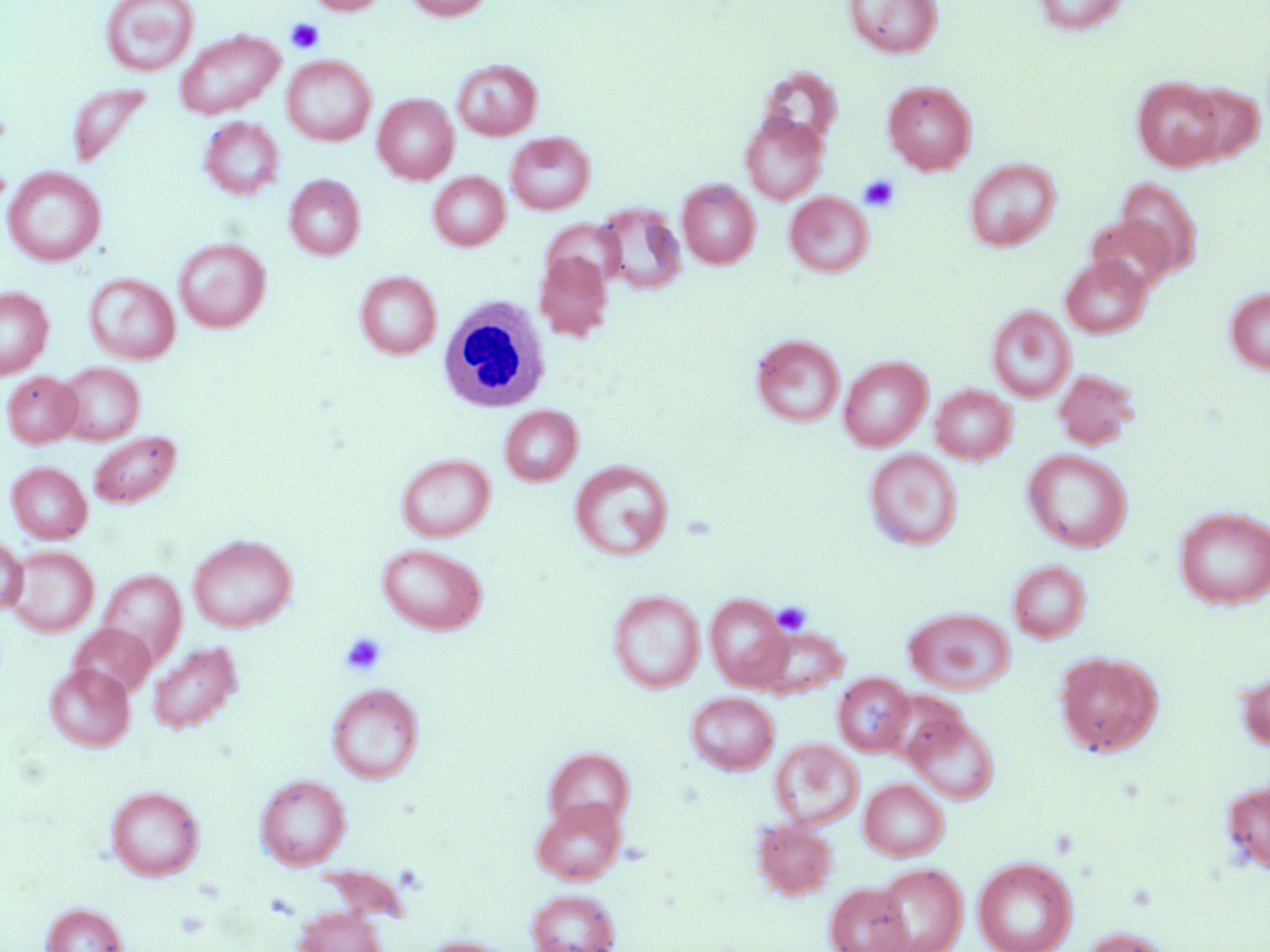

Summary:
  - Coordinate format: approximate bounding boxes as (x1, y1, x2, y2) in pixels
  - Platelet locations: (285, 18, 323, 54), (858, 175, 899, 212), (772, 601, 812, 636), (340, 631, 387, 676)
  - White blood cell locations: (437, 296, 550, 413)
  - Uninfected red blood cell locations: (100, 0, 198, 76), (308, 0, 388, 15), (405, 0, 493, 20), (843, 0, 943, 58), (1032, 0, 1127, 36), (175, 29, 284, 119), (281, 55, 376, 146), (452, 59, 542, 140), (756, 66, 844, 151), (1132, 77, 1224, 170), (882, 81, 977, 175), (1183, 83, 1264, 164), (65, 84, 155, 169), (373, 94, 460, 184), (740, 114, 828, 205), (199, 117, 284, 200), (505, 132, 596, 215), (964, 158, 1061, 251), (2, 166, 106, 266), (428, 172, 510, 250), (284, 174, 365, 260), (1116, 177, 1203, 276), (678, 180, 760, 268), (785, 192, 874, 277), (595, 202, 687, 296), (1087, 216, 1177, 294), (540, 218, 625, 291), (173, 238, 270, 332), (534, 251, 614, 341), (1060, 256, 1151, 339), (355, 271, 441, 359), (84, 274, 180, 364), (0, 286, 54, 379), (1225, 287, 1270, 375), (987, 305, 1076, 402), (751, 335, 846, 427), (839, 356, 932, 451), (55, 362, 145, 445), (1053, 369, 1139, 450), (2, 370, 82, 447), (930, 384, 1017, 464), (500, 405, 583, 486), (88, 431, 182, 508), (864, 449, 963, 550), (1023, 449, 1132, 552), (396, 453, 495, 542), (570, 460, 673, 561), (7, 462, 91, 543), (1174, 506, 1270, 610), (187, 534, 297, 632), (0, 536, 27, 614), (377, 542, 487, 634), (5, 545, 99, 637), (1008, 560, 1091, 643), (96, 569, 187, 666), (607, 590, 704, 693), (705, 594, 792, 691), (904, 608, 1016, 694), (67, 624, 157, 699), (757, 627, 848, 697), (148, 641, 242, 734), (1054, 650, 1164, 757), (44, 664, 135, 752), (1235, 669, 1270, 753), (833, 674, 914, 756), (326, 683, 424, 784), (884, 691, 966, 765), (685, 692, 779, 775), (908, 714, 1000, 805), (769, 739, 864, 831), (544, 748, 636, 832), (256, 774, 351, 870), (866, 777, 954, 952), (859, 778, 949, 861), (1221, 780, 1270, 876), (105, 785, 205, 881), (531, 797, 627, 885), (752, 818, 839, 901), (973, 857, 1077, 952), (872, 863, 966, 952), (824, 882, 912, 952), (526, 888, 621, 952), (40, 903, 127, 952), (293, 906, 388, 952), (1079, 927, 1172, 952), (421, 936, 510, 952)
  - Slide-level diagnosis: negative for blood parasites
  - Preparation: thin blood smear
  - Stain: May-Grünwald-Giemsa
  - Magnification: 1000x
  - Image size: 1270×952 pixels
  - Modality: optical microscopy
  - Field of view: single